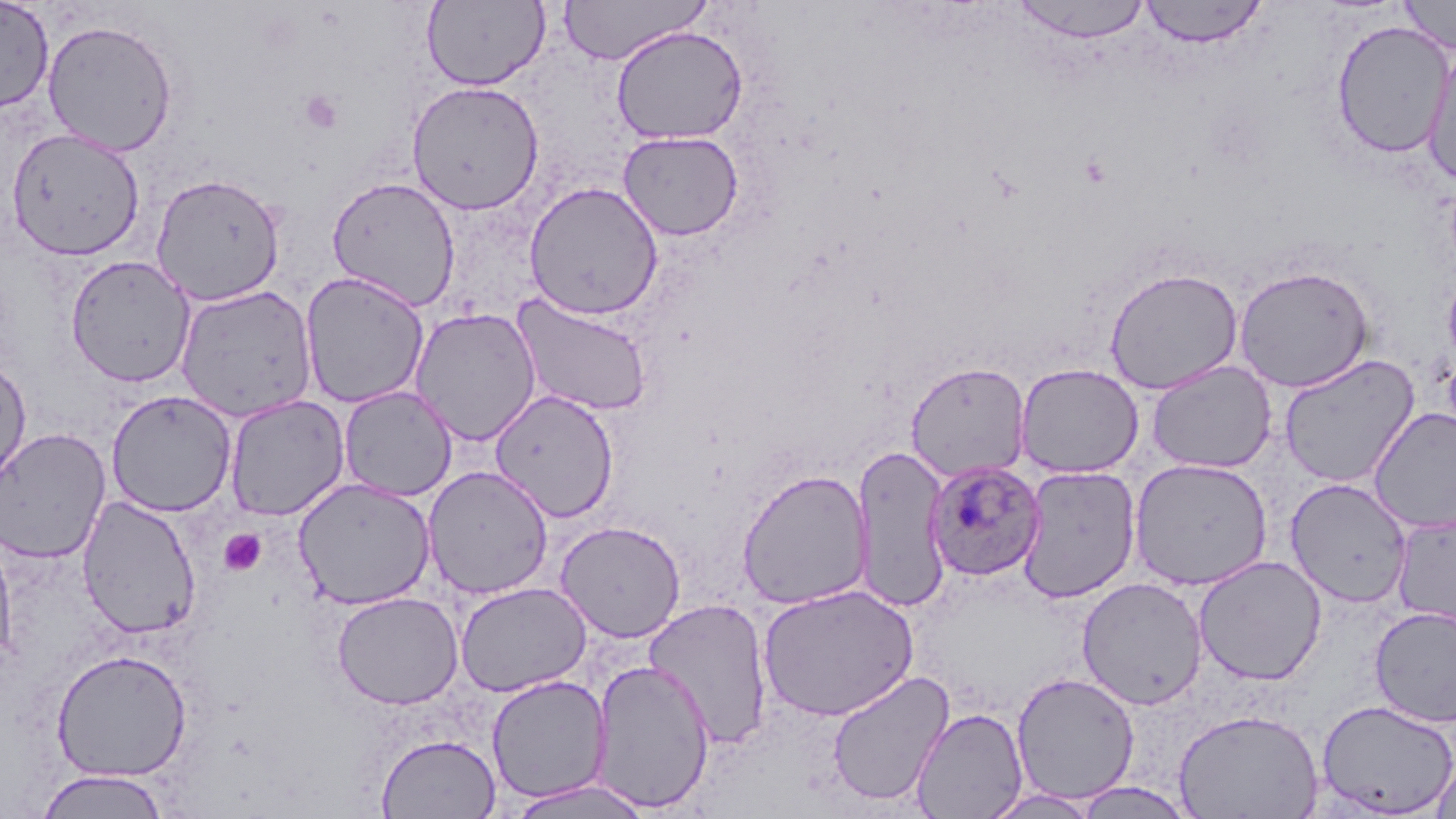
Approximate bounding boxes as (x1,y1)-(x2,y2) corner pairs in pixels. Uninfected red blood cell locations: (0,0)-(54,112), (558,0)-(711,65), (1138,0)-(1269,48), (1397,0)-(1456,55), (422,1)-(549,91), (1010,1)-(1153,43), (41,19)-(178,156), (1332,19)-(1453,159), (611,25)-(748,145), (1422,40)-(1456,186), (406,79)-(545,215), (5,127)-(146,260), (618,130)-(745,241), (150,173)-(287,306), (326,176)-(461,311), (524,181)-(664,320), (65,254)-(197,387), (1233,265)-(1374,392), (1104,267)-(1244,395), (1441,267)-(1456,376), (300,271)-(430,409), (175,283)-(318,422), (510,293)-(655,416), (409,306)-(542,446), (1278,353)-(1420,488), (0,356)-(32,487), (1147,360)-(1277,474), (905,362)-(1031,483), (1015,363)-(1143,478), (339,385)-(457,501), (489,389)-(620,522), (105,390)-(237,518), (224,395)-(350,521), (1368,407)-(1456,533), (0,428)-(112,564), (849,446)-(953,611), (1128,457)-(1273,591), (1017,465)-(1141,603), (422,466)-(554,600), (736,468)-(873,610), (292,477)-(436,610), (1285,477)-(1413,608), (77,495)-(201,640), (1391,513)-(1456,632), (554,520)-(687,643), (0,533)-(17,669), (1193,555)-(1327,686), (1076,577)-(1208,710), (455,582)-(591,697), (758,583)-(918,722), (331,591)-(464,710), (643,597)-(774,750), (1369,606)-(1456,726), (50,648)-(192,782), (590,659)-(715,813), (827,670)-(955,808), (1011,671)-(1140,804), (486,676)-(611,803), (1316,699)-(1456,816), (911,706)-(1029,819), (1173,709)-(1324,819), (377,734)-(501,818), (1430,755)-(1456,819), (34,769)-(171,818), (508,778)-(654,819), (1071,780)-(1198,817), (982,788)-(1100,818). Platelet locations: (299,90)-(344,134), (219,529)-(267,577). Plasmodium ovale-infected red blood cell locations: (925,460)-(1046,581). Slide-level diagnosis: Plasmodium ovale. Image is 1456×819 pixels. May-Grünwald-Giemsa stain. Single field of view. Captured at 1000x magnification. Light microscopy. Thin blood film.